Classify this cell by malaria status.
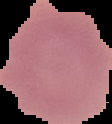
Uninfected.

From a thin blood film. Image is 112×124 pixels. Segmented cell region on a black background.